Report the malaria status of this cell.
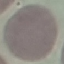

Uninfected.

stain = Giemsa
capture = smartphone through the microscope eyepiece
preparation = thin smear
image type = automatically extracted cell patch, resized to 64 × 64 pixels